Classify this cell by malaria status.
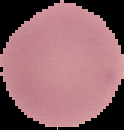
It is uninfected.

From a thin blood film. Image is 124×130 pixels. Cell region segmented out of the field of view; the surrounding area is masked to black.